Name the parasite shown.
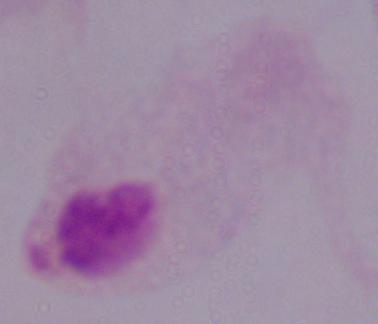
A trichomonad.

Captured at 1000x magnification. Micrograph.